Outline each uninfected red blood cell.
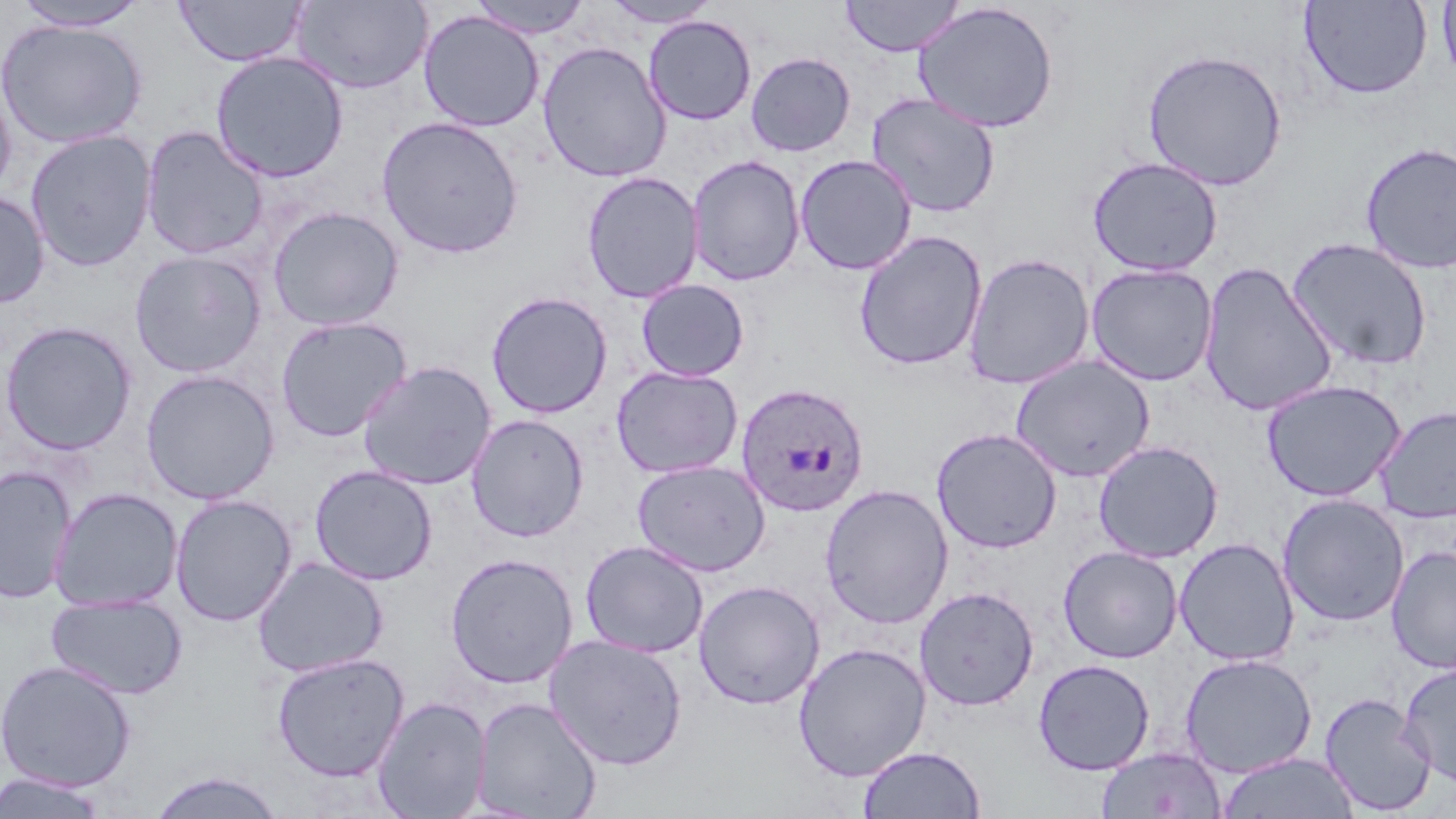
Approximate bounding boxes as [x1, y1, x2, y2] in pixels.
Uninfected red blood cells: [10, 0, 148, 30], [467, 0, 593, 38], [601, 0, 721, 28], [840, 0, 965, 57], [1436, 0, 1456, 88], [174, 1, 307, 67], [292, 1, 432, 94], [1299, 1, 1432, 100], [912, 2, 1060, 134], [418, 10, 545, 132], [643, 15, 757, 125], [0, 18, 148, 148], [536, 41, 672, 183], [1141, 48, 1287, 191], [210, 50, 349, 182], [745, 51, 856, 157], [0, 73, 17, 203], [866, 93, 1001, 218], [376, 116, 524, 259], [139, 126, 269, 260], [24, 129, 157, 272], [1359, 142, 1456, 275], [794, 154, 917, 275], [687, 155, 806, 286], [1087, 156, 1223, 276], [582, 171, 704, 304], [0, 189, 50, 308], [267, 206, 404, 331], [854, 230, 988, 371], [1287, 236, 1434, 372], [129, 251, 265, 378], [963, 252, 1096, 390], [1199, 261, 1338, 417], [1086, 263, 1219, 386], [636, 279, 750, 382], [486, 291, 613, 419], [275, 316, 412, 442], [0, 321, 137, 455], [1010, 355, 1156, 483], [357, 361, 497, 490], [611, 365, 743, 479], [140, 369, 280, 505], [1261, 379, 1406, 502], [1375, 405, 1456, 524], [466, 414, 589, 543], [931, 427, 1063, 554], [1093, 440, 1223, 563], [632, 459, 771, 576], [0, 465, 77, 603], [310, 465, 437, 586], [819, 484, 954, 630], [50, 488, 183, 612], [170, 494, 297, 627], [1277, 494, 1410, 627], [1174, 537, 1300, 666], [580, 540, 709, 658], [1386, 545, 1456, 673], [1058, 546, 1183, 663], [444, 552, 579, 689], [253, 557, 389, 677], [694, 580, 825, 710], [915, 586, 1039, 711], [47, 593, 187, 700], [543, 634, 688, 770], [793, 642, 932, 781], [271, 652, 410, 782], [1180, 653, 1318, 778], [1032, 658, 1155, 775], [0, 659, 136, 791], [1397, 662, 1456, 787], [1319, 692, 1436, 816], [372, 696, 491, 818], [472, 696, 602, 818], [857, 745, 986, 818], [1095, 747, 1227, 818], [1217, 752, 1360, 819], [145, 770, 288, 818], [0, 772, 111, 818].

Summary:
  - Plasmodium ovale-infected red blood cell locations: [734, 382, 871, 518]
  - Slide-level diagnosis: Plasmodium ovale
  - Modality: light microscopy
  - Field of view: single
  - Preparation: thin blood film
  - Magnification: 1000x
  - Stain: May-Grünwald-Giemsa
  - Image size: 1456×819 pixels